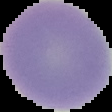
From a thin blood smear. Malaria status: uninfected. Image is 112×112 pixels. Segmented cell region on a black background.